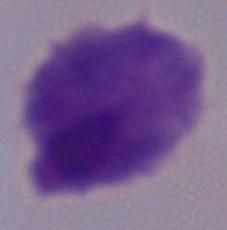

magnification: 1000x
modality: micrograph
identification: trichomonad